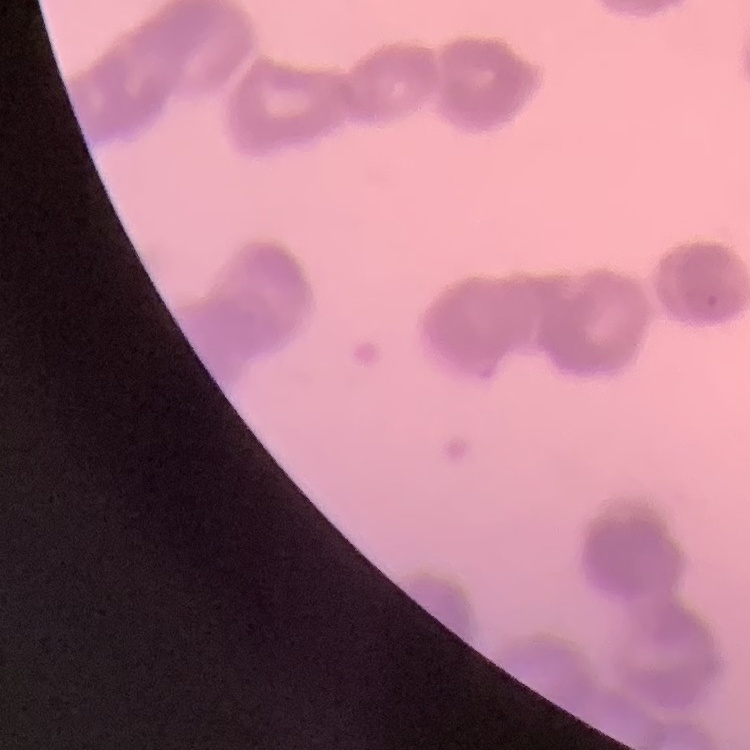

{
  "erythrocyte_morphology": "rouleaux formation",
  "stain": "Field's or Giemsa",
  "image_type": "one tile cut from a larger photomicrograph",
  "preparation": "thin blood smear"
}